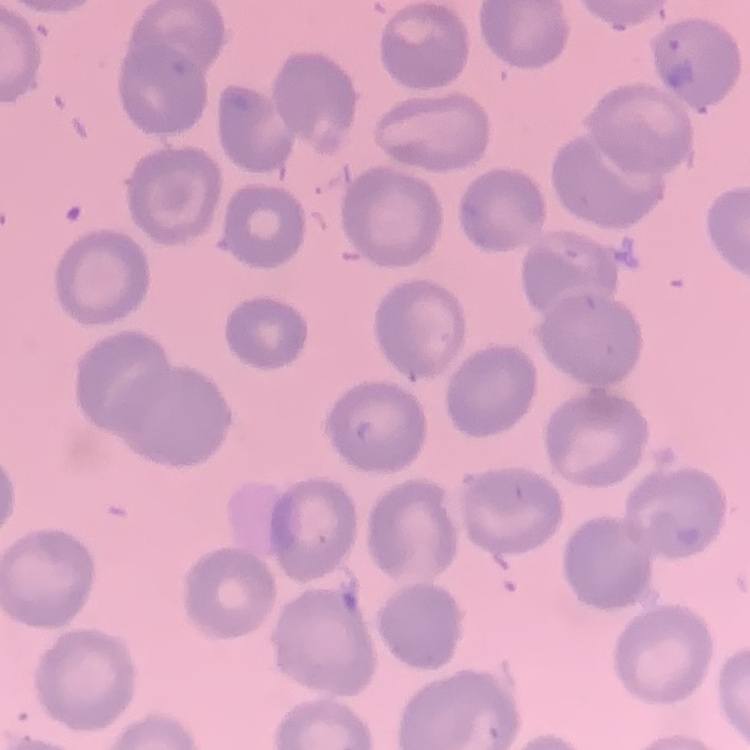

{
  "erythrocyte_morphology": "no rouleaux formation",
  "preparation": "thin blood smear",
  "stain": "Field's or Giemsa",
  "image_type": "one tile cut from a larger photomicrograph"
}